Classify this cell by malaria status.
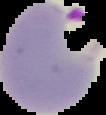
Parasitized.

Summary:
  - Image size: 106×115 pixels
  - Image type: cell region segmented out of the field of view; surrounding area masked to black
  - Preparation: thin blood smear